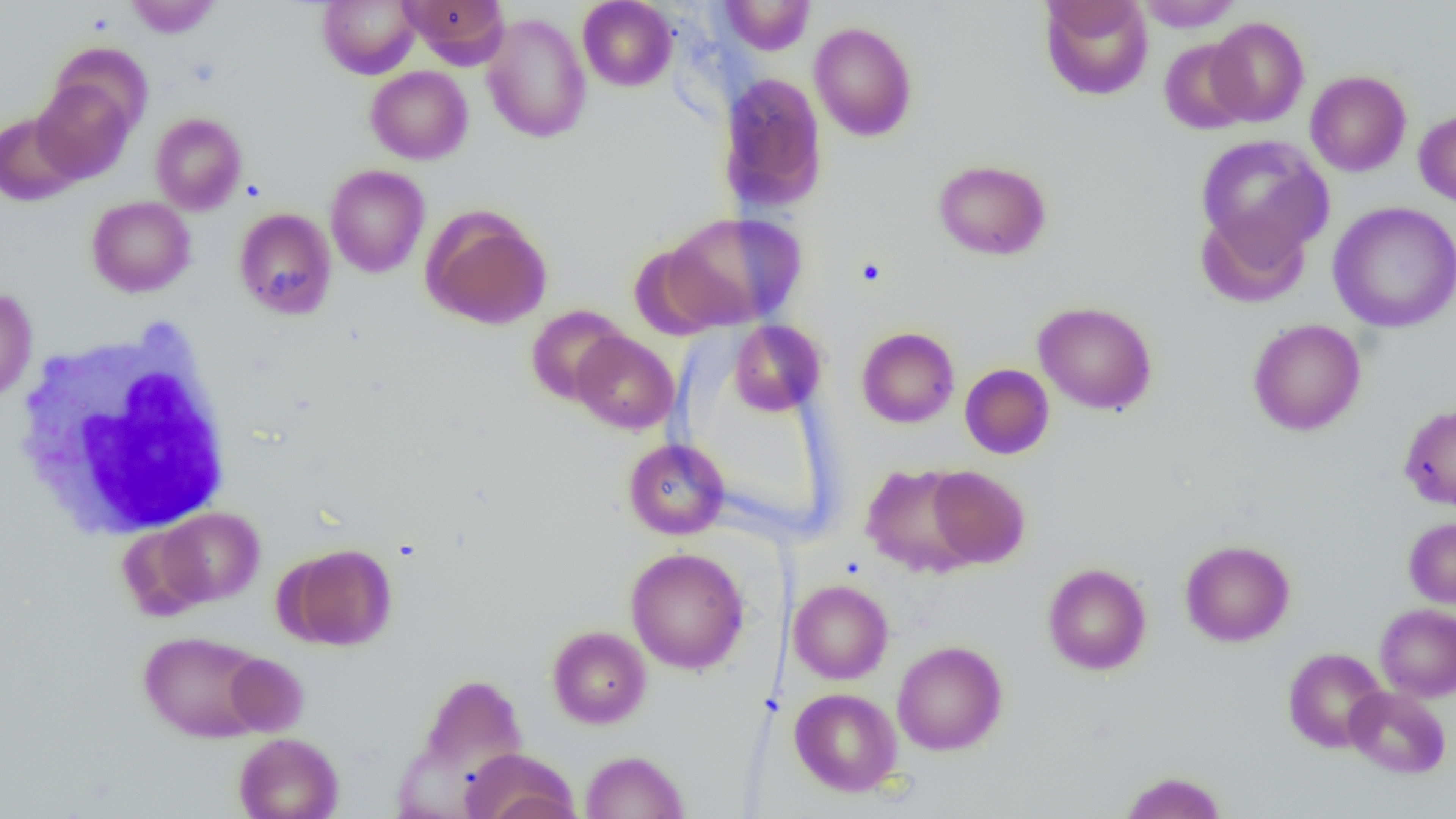
{
  "slide_level_diagnosis": "negative for blood parasites",
  "uninfected_red_blood_cell_locations": "approximate bounding boxes as [x1, y1, x2, y2] in pixels: [125, 0, 221, 38], [317, 0, 420, 79], [400, 0, 509, 66], [577, 0, 677, 91], [719, 0, 815, 55], [1040, 0, 1153, 100], [1135, 0, 1244, 31], [481, 12, 592, 143], [1207, 16, 1309, 127], [809, 21, 918, 141], [1159, 38, 1254, 135], [48, 41, 154, 136], [365, 65, 473, 165], [1305, 70, 1411, 176], [717, 72, 828, 213], [32, 79, 136, 183], [1414, 109, 1456, 207], [0, 112, 81, 206], [150, 112, 247, 215], [1196, 134, 1332, 257], [933, 159, 1052, 260], [325, 164, 430, 278], [86, 196, 195, 297], [1328, 201, 1456, 333], [1196, 206, 1311, 308], [422, 207, 552, 330], [234, 208, 337, 319], [662, 211, 807, 330], [0, 287, 37, 405], [1032, 301, 1158, 415], [526, 305, 630, 406], [1247, 318, 1366, 436], [729, 320, 825, 416], [857, 327, 960, 428], [571, 331, 679, 434], [960, 364, 1054, 459], [1399, 403, 1456, 510], [623, 438, 730, 539], [861, 463, 979, 576], [927, 467, 1030, 568], [157, 507, 264, 606], [1404, 517, 1456, 608], [116, 524, 211, 620], [1180, 540, 1295, 646], [284, 543, 397, 650], [625, 546, 749, 675], [1042, 563, 1152, 675], [788, 580, 893, 684], [1375, 603, 1456, 702], [547, 625, 651, 729], [138, 631, 269, 742], [892, 640, 1008, 755], [1283, 648, 1388, 753], [224, 654, 308, 735], [415, 673, 528, 783], [1345, 686, 1451, 778], [789, 688, 902, 796], [234, 732, 343, 819], [460, 748, 578, 819], [581, 750, 689, 818], [1119, 771, 1227, 819]",
  "image_size": "1456×819 pixels",
  "white_blood_cell_locations": "approximate bounding boxes as [x1, y1, x2, y2] in pixels: [11, 321, 237, 541]",
  "magnification": "1000x",
  "modality": "light microscopy",
  "preparation": "thin blood film",
  "field_of_view": "single"
}